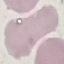
{
  "malaria_status": "uninfected",
  "stain": "Giemsa",
  "preparation": "thin blood film",
  "image_type": "cell patch, automatically extracted from a larger field of view and resized to 64 × 64 pixels",
  "capture": "smartphone camera at the microscope eyepiece"
}